Locate every blood parasite and identify its species.
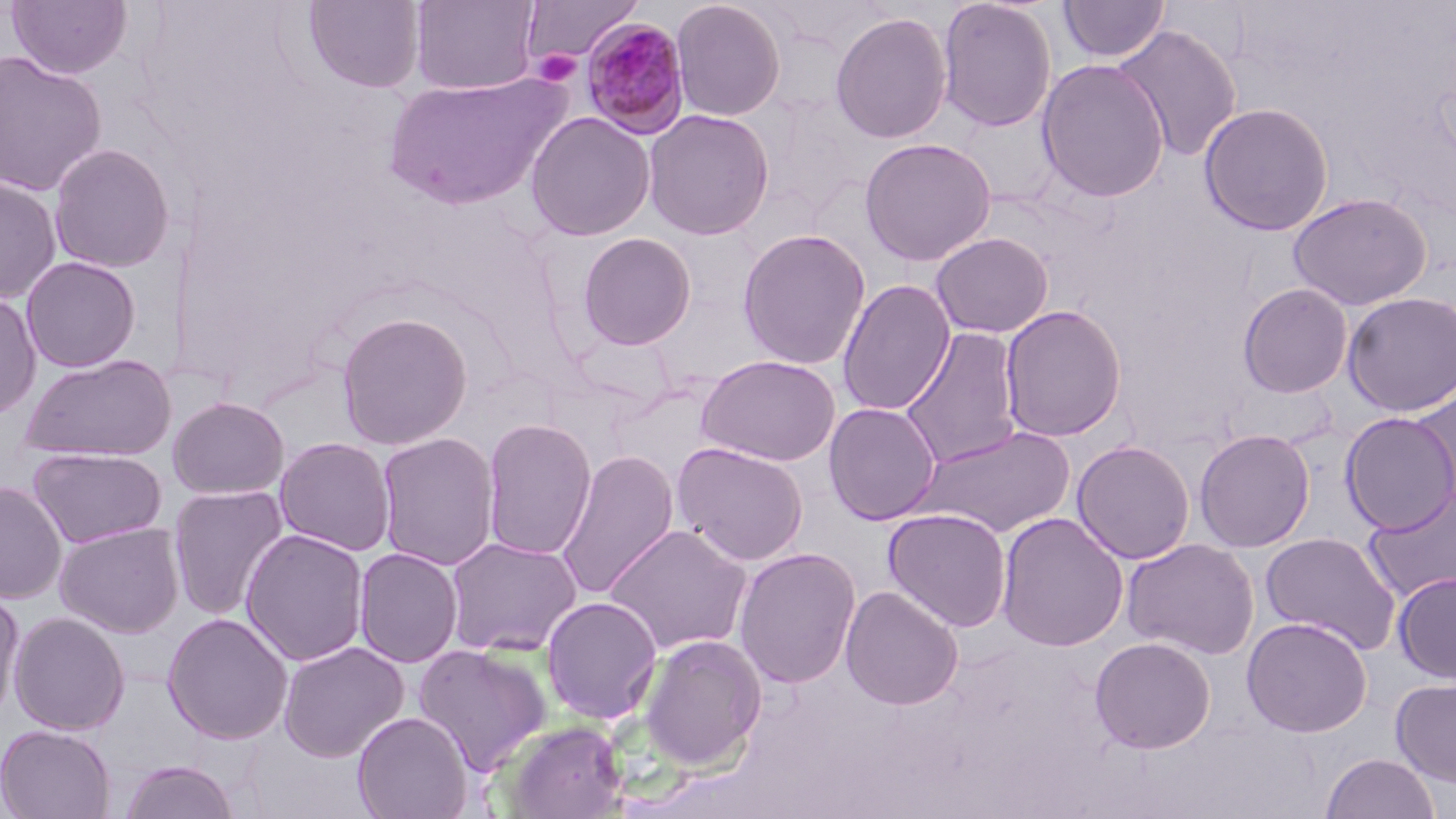

Approximate bounding boxes as (x1,y1)-(x2,y2) corner pairs in pixels.
Plasmodium malariae-infected red blood cells: (580,18)-(691,139).
No Plasmodium falciparum, Plasmodium ovale, Plasmodium vivax, Babesia divergens, or Trypanosoma brucei observed.

slide-level diagnosis = Plasmodium malariae
field of view = one of a larger specimen
stain = May-Grünwald-Giemsa
uninfected red blood cell locations = approximate bounding boxes as (x1,y1)-(x2,y2) corner pairs in pixels: (5,0)-(133,79), (409,0)-(540,95), (521,0)-(642,64), (670,0)-(787,121), (937,0)-(1057,132), (1058,0)-(1169,63), (301,1)-(426,94), (830,11)-(953,144), (1112,24)-(1243,162), (0,50)-(107,197), (1036,58)-(1169,202), (381,71)-(571,209), (758,91)-(870,227), (1199,101)-(1334,236), (642,108)-(776,241), (525,111)-(656,241), (859,137)-(997,266), (48,143)-(176,273), (0,176)-(62,304), (1287,192)-(1432,310), (737,228)-(871,369), (576,232)-(698,350), (931,232)-(1054,338), (20,256)-(141,373), (837,279)-(956,416), (1237,282)-(1354,398), (0,292)-(42,420), (1342,292)-(1455,416), (1000,305)-(1127,442), (335,311)-(473,450), (900,326)-(1024,470), (19,353)-(177,462), (696,354)-(841,466), (1408,387)-(1456,513), (167,396)-(289,499), (823,402)-(942,525), (1340,411)-(1456,534), (481,417)-(597,560), (910,424)-(1077,538), (1194,428)-(1315,552), (376,431)-(501,571), (274,436)-(397,557), (1072,440)-(1196,564), (672,441)-(809,566), (27,446)-(167,549), (556,449)-(680,600), (0,481)-(67,603), (167,485)-(289,621), (1363,485)-(1456,604), (883,507)-(1013,632), (995,512)-(1129,652), (54,521)-(185,638), (604,524)-(753,656), (241,528)-(370,666), (1260,531)-(1402,654), (444,536)-(583,657), (1122,538)-(1260,660), (733,546)-(862,689), (353,547)-(463,668), (1393,571)-(1456,684), (840,585)-(964,710), (0,588)-(25,723), (540,595)-(664,724), (8,611)-(130,736), (162,612)-(293,744), (1241,616)-(1373,737), (638,633)-(767,771), (1089,636)-(1216,754), (278,640)-(409,762), (413,643)-(552,775), (1390,676)-(1456,787), (351,711)-(473,819), (499,719)-(629,818), (0,724)-(116,819), (1320,752)-(1439,819), (117,758)-(241,819)
magnification = 1000x
platelet locations = approximate bounding boxes as (x1,y1)-(x2,y2) corner pairs in pixels: (531,49)-(582,87)
modality = optical microscopy
preparation = thin blood smear
image size = 1456×819 pixels